Classify this cell by malaria status.
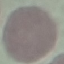

Uninfected.

Photographed with a smartphone camera at the microscope eyepiece. Thin smear of blood. Cell patch, automatically extracted from a larger field of view and resized to 64 × 64 pixels. Giemsa stain.